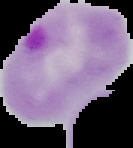

preparation = thin blood film
malaria status = parasitized
image size = 133×148 pixels
image type = segmented cell region on a black background